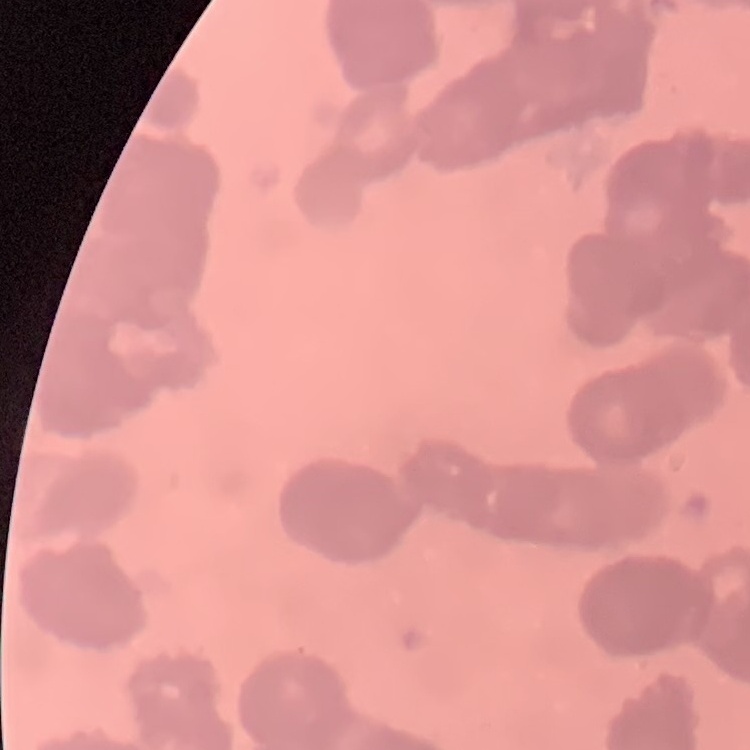

The erythrocytes exhibit rouleaux formation. Thin peripheral smear. Field's or Giemsa stain. One tile cut from a larger photomicrograph.